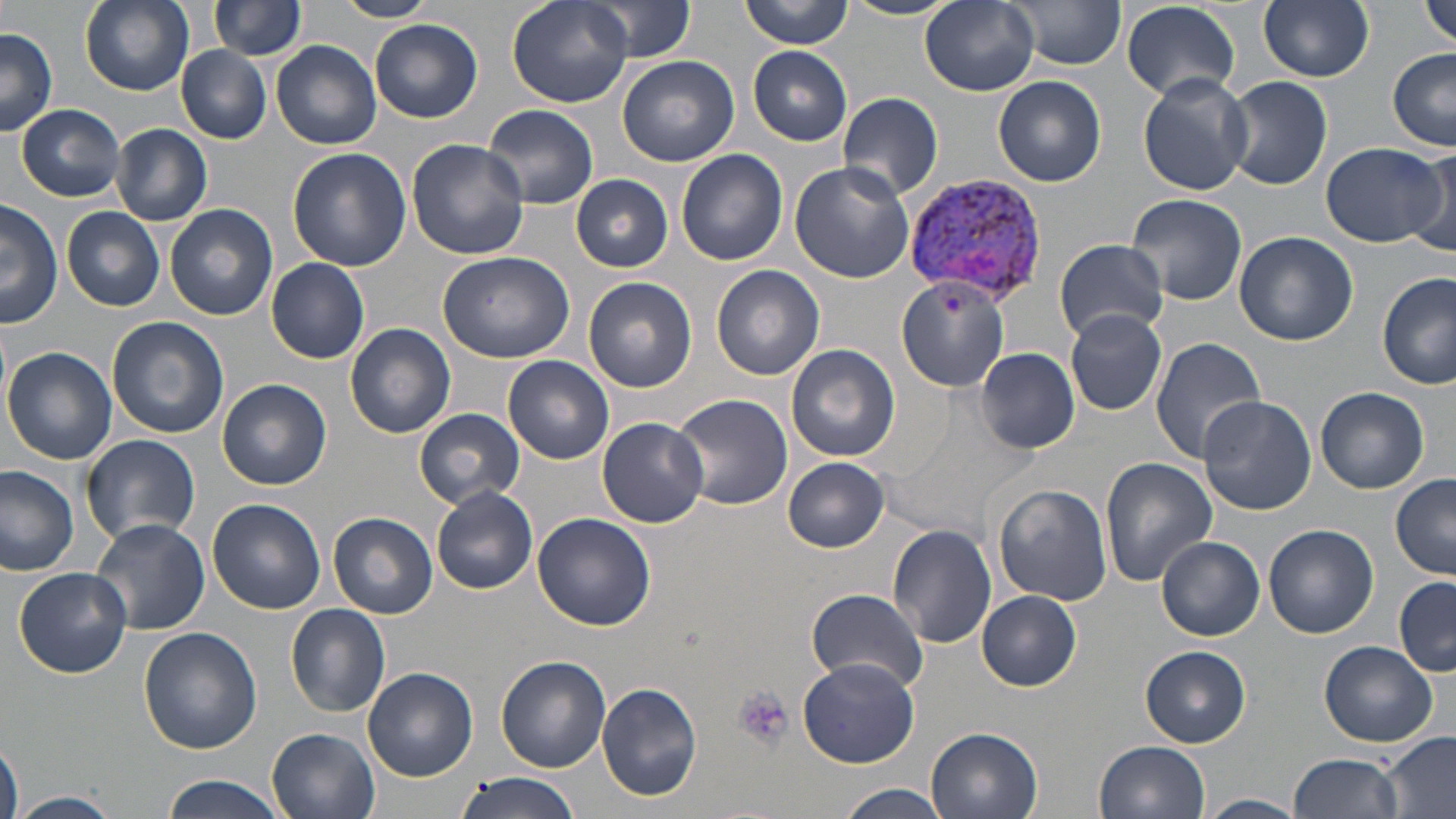

Approximate bounding boxes as named x1/y1/x2/y2 corners in pixels. Plasmodium vivax-infected red blood cell locations: (x1=902, y1=173, x2=1052, y2=305). Platelet locations: (x1=734, y1=686, x2=793, y2=753). Uninfected red blood cell locations: (x1=79, y1=0, x2=195, y2=94), (x1=210, y1=0, x2=306, y2=59), (x1=335, y1=0, x2=436, y2=23), (x1=509, y1=0, x2=631, y2=108), (x1=580, y1=0, x2=699, y2=61), (x1=741, y1=0, x2=853, y2=49), (x1=1007, y1=0, x2=1129, y2=69), (x1=1258, y1=0, x2=1374, y2=83), (x1=1422, y1=0, x2=1456, y2=49), (x1=839, y1=1, x2=958, y2=21), (x1=920, y1=1, x2=1040, y2=97), (x1=1120, y1=2, x2=1242, y2=101), (x1=370, y1=20, x2=482, y2=123), (x1=0, y1=26, x2=58, y2=136), (x1=272, y1=39, x2=382, y2=149), (x1=177, y1=45, x2=271, y2=142), (x1=749, y1=46, x2=852, y2=145), (x1=1388, y1=49, x2=1456, y2=150), (x1=617, y1=54, x2=740, y2=167), (x1=1138, y1=72, x2=1252, y2=196), (x1=994, y1=75, x2=1106, y2=186), (x1=1223, y1=75, x2=1333, y2=190), (x1=836, y1=91, x2=943, y2=203), (x1=16, y1=104, x2=127, y2=201), (x1=482, y1=104, x2=600, y2=210), (x1=112, y1=124, x2=212, y2=226), (x1=406, y1=138, x2=529, y2=260), (x1=1319, y1=141, x2=1446, y2=247), (x1=1411, y1=145, x2=1456, y2=254), (x1=287, y1=148, x2=411, y2=272), (x1=676, y1=149, x2=788, y2=266), (x1=788, y1=160, x2=916, y2=283), (x1=571, y1=173, x2=674, y2=272), (x1=1126, y1=193, x2=1247, y2=307), (x1=1, y1=196, x2=64, y2=327), (x1=164, y1=204, x2=278, y2=321), (x1=62, y1=206, x2=165, y2=311), (x1=1234, y1=230, x2=1358, y2=346), (x1=1055, y1=238, x2=1169, y2=342), (x1=436, y1=250, x2=576, y2=365), (x1=267, y1=258, x2=370, y2=364), (x1=712, y1=266, x2=825, y2=380), (x1=1377, y1=272, x2=1455, y2=390), (x1=896, y1=275, x2=1013, y2=393), (x1=583, y1=277, x2=697, y2=393), (x1=1063, y1=309, x2=1168, y2=414), (x1=107, y1=316, x2=230, y2=439), (x1=345, y1=322, x2=457, y2=439), (x1=1150, y1=335, x2=1268, y2=464), (x1=786, y1=343, x2=899, y2=461), (x1=4, y1=347, x2=118, y2=464), (x1=975, y1=347, x2=1081, y2=454), (x1=504, y1=355, x2=614, y2=465), (x1=219, y1=379, x2=333, y2=491), (x1=1315, y1=387, x2=1429, y2=494), (x1=670, y1=393, x2=793, y2=510), (x1=1197, y1=395, x2=1317, y2=514), (x1=415, y1=407, x2=526, y2=509), (x1=598, y1=416, x2=708, y2=528), (x1=80, y1=434, x2=202, y2=546), (x1=784, y1=457, x2=889, y2=552), (x1=1099, y1=457, x2=1216, y2=585), (x1=0, y1=464, x2=80, y2=575), (x1=1390, y1=474, x2=1456, y2=579), (x1=992, y1=483, x2=1113, y2=606), (x1=432, y1=486, x2=537, y2=596), (x1=207, y1=499, x2=326, y2=614), (x1=329, y1=512, x2=438, y2=620), (x1=533, y1=512, x2=654, y2=631), (x1=91, y1=518, x2=210, y2=636), (x1=1263, y1=523, x2=1378, y2=638), (x1=887, y1=524, x2=997, y2=648), (x1=1156, y1=536, x2=1265, y2=642), (x1=13, y1=566, x2=132, y2=677), (x1=1395, y1=575, x2=1456, y2=674), (x1=807, y1=587, x2=928, y2=692), (x1=977, y1=591, x2=1083, y2=690), (x1=285, y1=604, x2=391, y2=717), (x1=139, y1=627, x2=263, y2=756), (x1=1320, y1=640, x2=1437, y2=747), (x1=1141, y1=646, x2=1251, y2=747), (x1=497, y1=654, x2=611, y2=772), (x1=796, y1=657, x2=922, y2=768), (x1=364, y1=667, x2=478, y2=782), (x1=597, y1=682, x2=702, y2=803), (x1=267, y1=728, x2=380, y2=819), (x1=926, y1=728, x2=1042, y2=819), (x1=1383, y1=730, x2=1456, y2=818), (x1=1095, y1=740, x2=1211, y2=819), (x1=0, y1=741, x2=23, y2=819), (x1=1287, y1=752, x2=1404, y2=819), (x1=454, y1=772, x2=581, y2=819), (x1=161, y1=774, x2=284, y2=819), (x1=837, y1=784, x2=952, y2=819), (x1=10, y1=790, x2=123, y2=818), (x1=1200, y1=795, x2=1306, y2=818). Slide-level diagnosis: Plasmodium vivax. Captured at 1000x magnification. Single field of view. Image is 1456×819 pixels. May-Grünwald-Giemsa stain. Thin blood film. Light microscopy.